Classify this cell by malaria status.
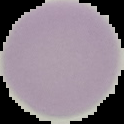
It is uninfected.

preparation = thin blood film
image size = 124×124 pixels
image type = segmented cell region on a black background